Report the malaria status of this cell.
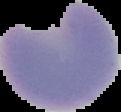

It is parasitized.

Summary:
  - Preparation: thin blood smear
  - Image type: cell region segmented out of the field of view; surrounding area masked to black
  - Image size: 121×112 pixels